Identify the parasite.
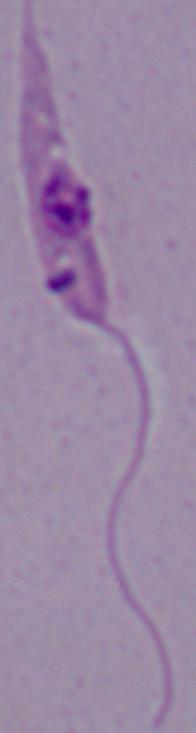

Leishmania.

1000x magnification. Photomicrograph.